Classify this cell by malaria status.
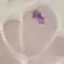

It is uninfected.

Summary:
  - Capture: smartphone through the microscope eyepiece
  - Preparation: thin blood film
  - Image type: automatically extracted cell patch, resized to 64 × 64 pixels
  - Stain: Giemsa